Point out each Plasmodium parasite.
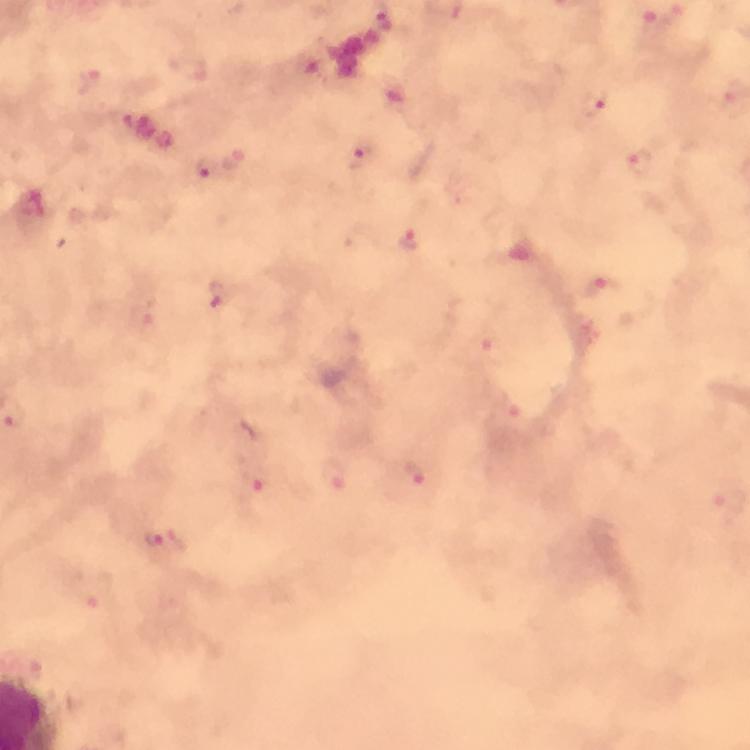
Approximate centers as {x, y} in pixels.
Plasmodium parasites: {384, 22}, {651, 26}, {91, 81}, {592, 107}, {361, 157}, {639, 160}, {206, 170}, {411, 238}, {603, 288}, {217, 295}, {490, 345}, {416, 475}, {336, 476}, {254, 481}, {163, 540}.

Cropped region of a single field of view. Immersion oil applied. Image is 750×750 pixels. 100x magnification. From a diagnostic examination for malaria. Giemsa-stained preparation. Smartphone photograph taken through a microscope. Thick blood film.